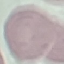

Result: negative for malaria parasites. Giemsa-stained preparation. Thin blood film. Automatically extracted cell patch, resized to 64 × 64 pixels. Acquired by smartphone through the microscope eyepiece.